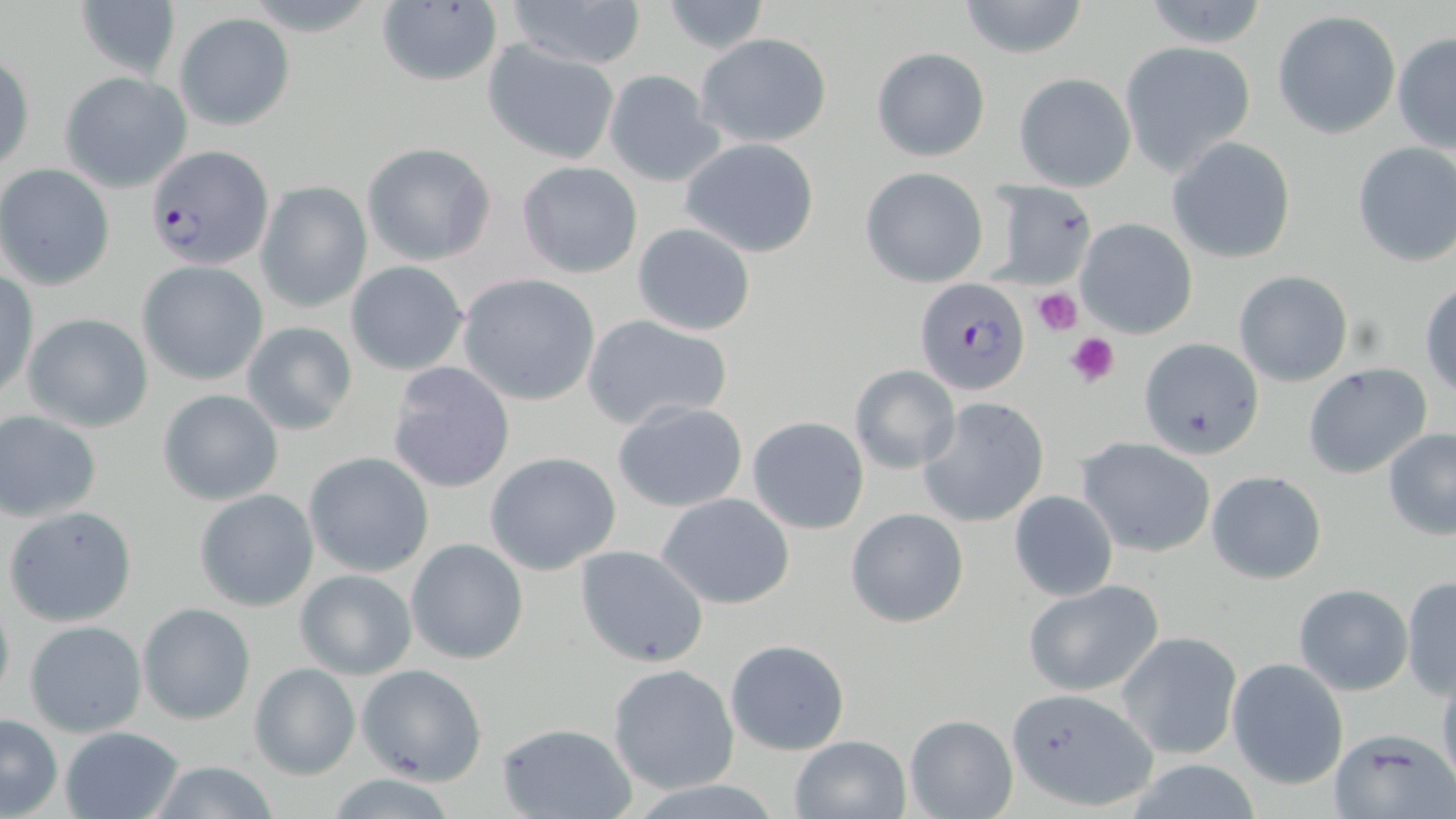
Summary:
  - Coordinate format: approximate bounding boxes as (x1,y1)-(x2,y2) corner pairs in pixels
  - Uninfected red blood cell locations: (72,0)-(181,78), (501,0)-(648,69), (658,0)-(771,53), (956,1)-(1090,59), (1138,1)-(1272,50), (375,2)-(504,88), (1272,10)-(1400,139), (175,12)-(296,130), (1392,31)-(1456,155), (695,32)-(833,149), (482,40)-(620,165), (1119,41)-(1256,175), (870,47)-(990,161), (1,49)-(33,177), (601,68)-(723,187), (60,71)-(192,192), (1013,73)-(1136,192), (680,137)-(822,257), (1167,137)-(1297,263), (1351,141)-(1456,267), (360,142)-(495,266), (515,161)-(644,279), (1,165)-(115,290), (860,167)-(988,287), (987,181)-(1098,287), (256,182)-(371,313), (1075,218)-(1198,339), (631,222)-(756,337), (138,261)-(270,385), (345,261)-(468,376), (1,270)-(38,399), (1233,271)-(1353,386), (458,272)-(601,406), (1420,280)-(1456,399), (23,312)-(153,432), (581,313)-(734,430), (240,320)-(358,435), (1139,337)-(1267,460), (387,361)-(516,494), (848,363)-(962,475), (1303,363)-(1435,480), (157,389)-(284,505), (920,397)-(1049,526), (611,400)-(750,513), (0,410)-(103,521), (747,415)-(870,534), (1381,429)-(1456,540), (1079,437)-(1215,558), (304,451)-(434,577), (485,451)-(622,575), (1206,469)-(1329,585), (193,488)-(320,611), (1008,490)-(1118,599), (655,491)-(795,609), (5,506)-(138,628), (845,507)-(970,629), (406,538)-(529,664), (575,544)-(709,668), (294,567)-(418,680), (1402,576)-(1456,699), (1024,578)-(1164,696), (1293,584)-(1412,696), (0,586)-(14,710), (137,603)-(255,724), (23,619)-(147,738), (1118,630)-(1243,760), (724,638)-(851,755), (1228,657)-(1349,789), (249,663)-(360,780), (608,663)-(742,796), (358,664)-(487,786), (1436,673)-(1456,795), (1004,688)-(1160,811), (0,712)-(63,817), (905,715)-(1017,819), (496,722)-(636,819), (60,727)-(185,819), (1331,727)-(1455,817), (789,735)-(911,819), (141,761)-(286,818), (324,774)-(457,818)
  - Platelet locations: (1032,285)-(1085,335), (1065,330)-(1120,387)
  - Plasmodium falciparum-infected red blood cell locations: (147,145)-(274,270), (913,277)-(1028,398)
  - Slide-level diagnosis: Plasmodium falciparum
  - Preparation: thin blood smear
  - Image size: 1456×819 pixels
  - Modality: optical microscopy
  - Field of view: one of a larger specimen
  - Magnification: 1000x
  - Stain: May-Grünwald-Giemsa